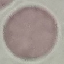
result: no malaria parasites detected
preparation: thin blood smear
capture: smartphone through the microscope eyepiece
image_type: cell patch, automatically extracted from a larger field of view and resized to 64 × 64 pixels
stain: Giemsa